State which parasite is depicted.
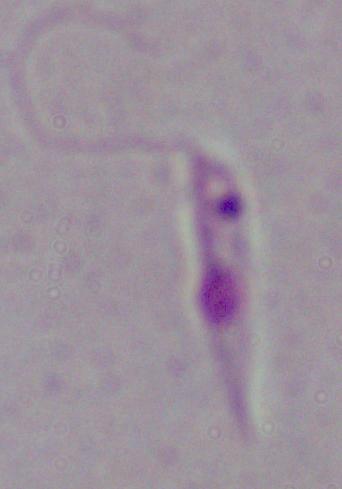
This is Leishmania.

modality: photomicrograph
magnification: 1000x